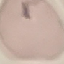 Malaria status: uninfected. Thin blood film. Giemsa stain. Cell patch, automatically extracted from a larger field of view and resized to 64 × 64 pixels. Photographed with a smartphone camera at the microscope eyepiece.